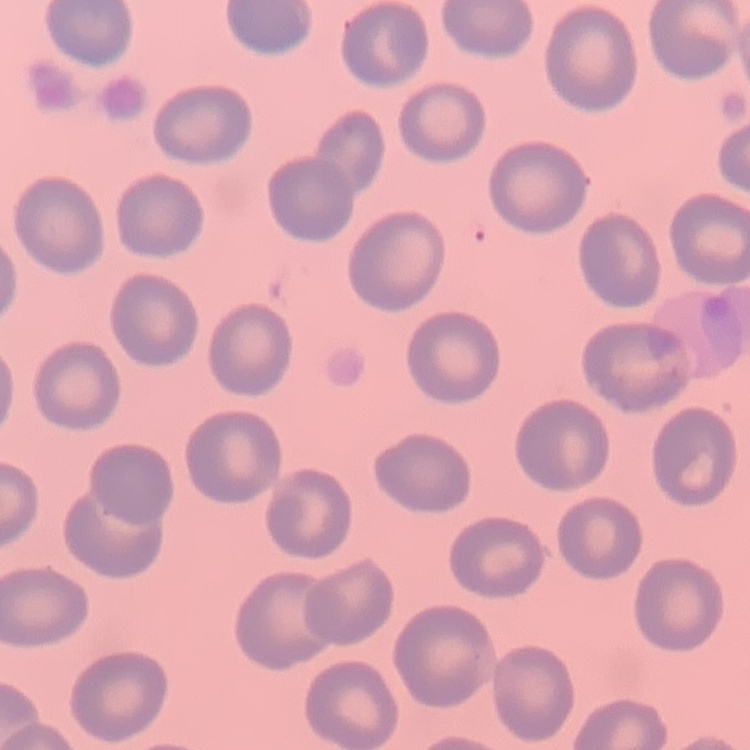

{
  "red_blood_cell_morphology": "no rouleaux formation",
  "preparation": "thin blood film",
  "stain": "Field's or Giemsa",
  "image_type": "square crop of a larger photomicrograph"
}